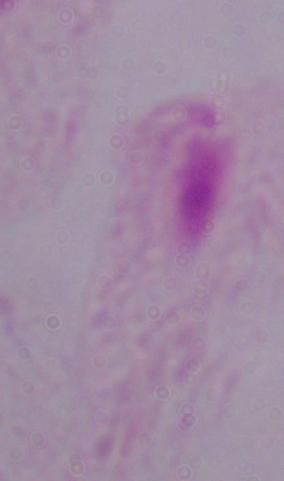

Photomicrograph. 1000x magnification. A trichomonad is seen.